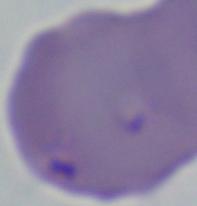 1000x magnification. A Babesia parasite is seen. Micrograph.